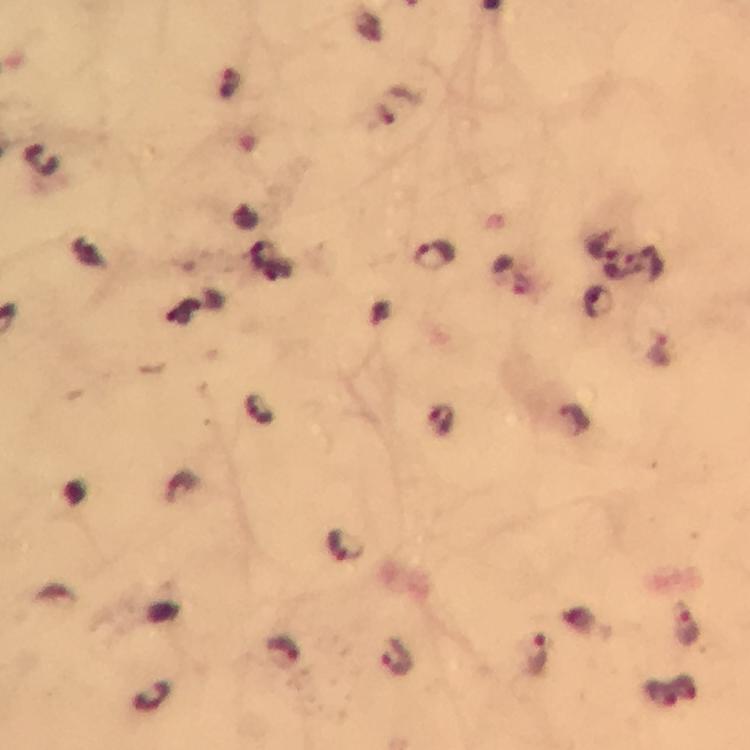 Approximate object centers, in pixels from the top-left corner. Plasmodium parasite locations: (x=434, y=256), (x=643, y=265), (x=616, y=266), (x=658, y=351), (x=259, y=410), (x=442, y=419), (x=572, y=420), (x=347, y=546), (x=686, y=624), (x=281, y=652), (x=534, y=657), (x=397, y=658). Photographed with a smartphone mounted on the microscope. Image is 750×750 pixels. 100x magnification. Thick blood smear. Immersion oil applied. A crop from one field of view. From a malaria diagnostic workup. Giemsa-stained preparation.